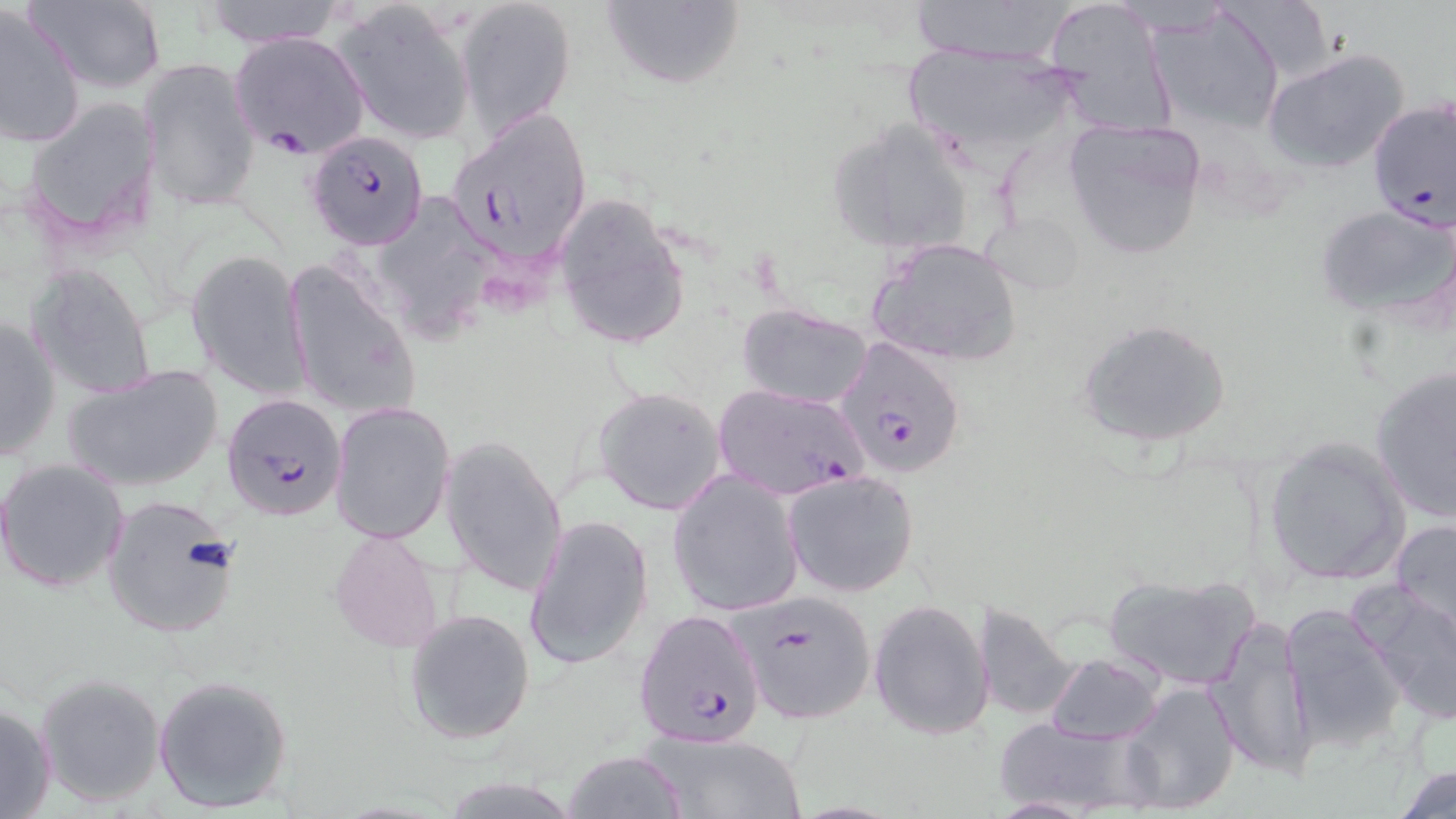
slide-level diagnosis = Plasmodium falciparum
stain = May-Grünwald-Giemsa
Plasmodium falciparum-infected red blood cell locations = approximate bounding boxes as (x1, y1, x2, y2) in pixels: (230, 31, 369, 156), (1368, 98, 1456, 237), (447, 109, 594, 265), (306, 128, 430, 249), (837, 338, 968, 479), (220, 393, 348, 522), (735, 590, 877, 724), (634, 609, 767, 748)
field of view = single
uninfected red blood cell locations = approximate bounding boxes as (x1, y1, x2, y2) in pixels: (26, 0, 169, 94), (198, 0, 345, 48), (456, 0, 576, 139), (599, 0, 745, 91), (906, 0, 1073, 63), (1041, 0, 1174, 135), (335, 1, 474, 144), (0, 5, 87, 151), (1149, 5, 1288, 136), (901, 43, 1083, 165), (1264, 47, 1411, 175), (138, 59, 262, 209), (21, 98, 161, 247), (1061, 116, 1208, 259), (829, 119, 978, 256), (555, 191, 690, 353), (1314, 201, 1455, 321), (868, 237, 1023, 366), (186, 248, 311, 400), (283, 258, 419, 423), (27, 263, 156, 402), (738, 304, 873, 409), (1, 312, 62, 464), (1077, 316, 1234, 450), (64, 364, 225, 493), (1370, 366, 1456, 523), (712, 382, 869, 500), (593, 386, 727, 516), (330, 402, 456, 546), (440, 433, 568, 599), (1262, 435, 1412, 586), (1, 458, 129, 593), (666, 469, 805, 617), (782, 469, 921, 598), (98, 493, 242, 640), (522, 513, 653, 671), (1389, 518, 1456, 644), (328, 525, 447, 656), (1102, 573, 1261, 690), (1355, 585, 1456, 728), (868, 598, 994, 739), (973, 602, 1080, 721), (1280, 603, 1406, 751), (403, 607, 535, 745), (1206, 612, 1314, 777), (1046, 653, 1166, 745), (34, 672, 167, 807), (154, 674, 294, 813), (1119, 681, 1241, 814), (0, 702, 57, 819), (991, 716, 1163, 817), (636, 728, 805, 817), (563, 750, 687, 819), (1389, 761, 1456, 818)
magnification = 1000x
image size = 1456×819 pixels
modality = optical microscopy
preparation = thin blood smear